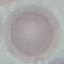
malaria_status: uninfected
preparation: thin smear
image_type: cell patch, automatically extracted from a larger field of view and resized to 64 × 64 pixels
capture: smartphone camera at the microscope eyepiece
stain: Giemsa